Locate every Plasmodium falciparum-infected red blood cell.
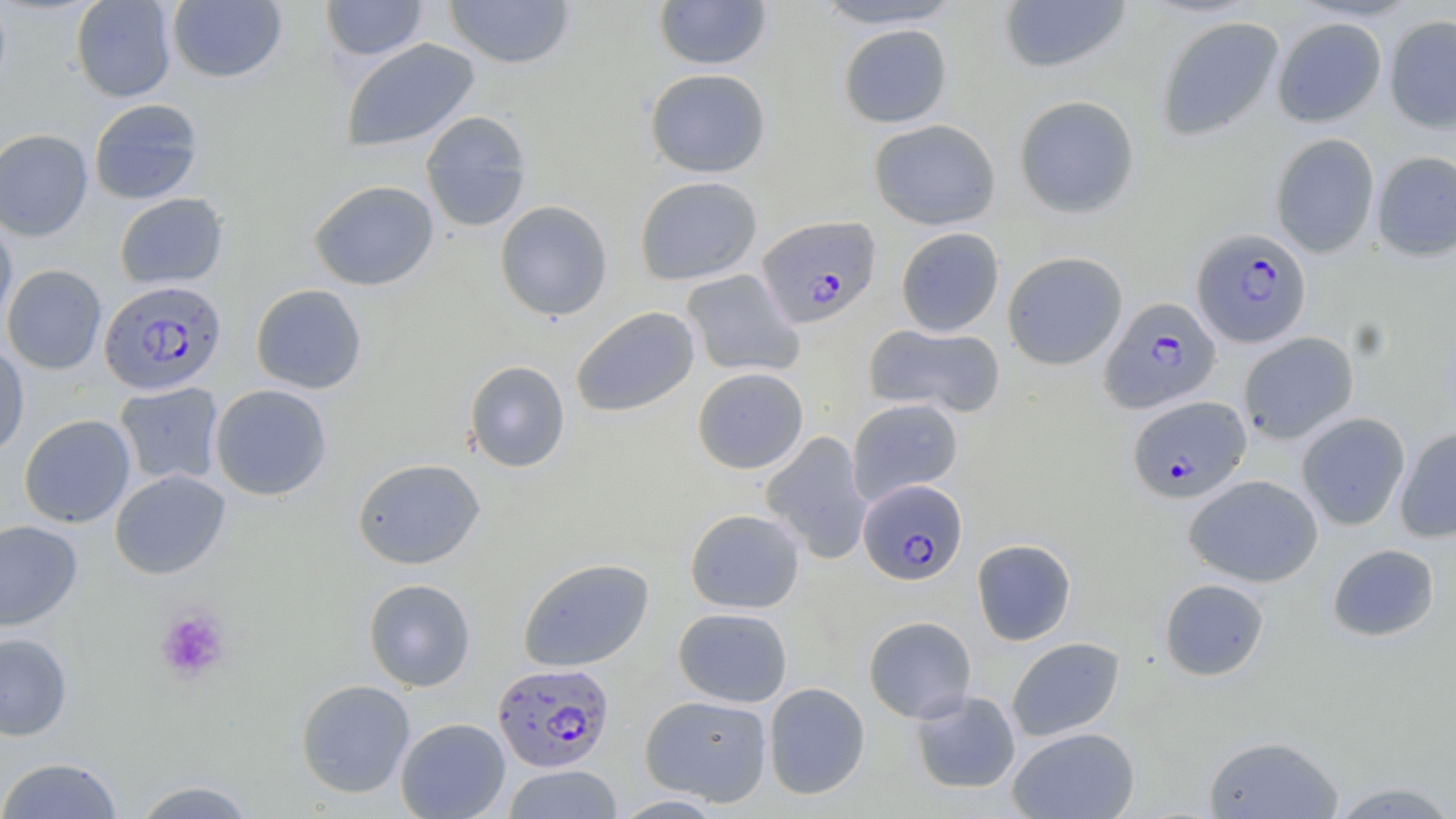
Approximate bounding boxes as (x1, y1, x2, y2) in pixels.
Plasmodium falciparum-infected red blood cells: (757, 215, 881, 328), (1191, 228, 1312, 348), (98, 280, 226, 395), (1100, 296, 1221, 414), (1127, 395, 1251, 504), (858, 479, 968, 586), (493, 661, 614, 772).

Uninfected red blood cell locations: (71, 0, 176, 102), (320, 0, 429, 61), (444, 0, 575, 69), (653, 0, 772, 70), (812, 0, 966, 29), (998, 0, 1132, 75), (167, 1, 286, 83), (1384, 15, 1456, 133), (1156, 16, 1284, 141), (1272, 17, 1387, 127), (838, 24, 952, 128), (340, 38, 480, 153), (645, 68, 771, 178), (1014, 95, 1140, 219), (88, 98, 204, 204), (420, 110, 532, 232), (869, 119, 1001, 230), (0, 129, 93, 241), (1270, 133, 1380, 258), (1372, 151, 1456, 261), (634, 175, 762, 286), (308, 179, 439, 291), (114, 192, 228, 290), (495, 200, 613, 321), (0, 217, 17, 329), (895, 227, 1004, 336), (1003, 251, 1128, 370), (2, 264, 107, 374), (681, 269, 804, 378), (250, 283, 367, 394), (571, 306, 700, 417), (864, 323, 1006, 418), (1238, 332, 1359, 444), (0, 341, 30, 458), (464, 360, 570, 473), (692, 367, 809, 473), (114, 382, 224, 487), (209, 384, 332, 501), (848, 397, 963, 504), (1296, 412, 1411, 530), (19, 414, 136, 528), (1395, 428, 1456, 543), (760, 431, 873, 563), (352, 457, 485, 570), (110, 469, 230, 579), (1184, 474, 1323, 587), (685, 508, 805, 613), (0, 520, 83, 631), (971, 539, 1077, 646), (1326, 543, 1440, 642), (517, 557, 654, 672), (363, 578, 476, 691), (1159, 578, 1270, 681), (673, 607, 793, 707), (863, 616, 977, 723), (0, 632, 73, 741), (1006, 637, 1125, 742), (295, 679, 415, 798), (763, 682, 870, 800), (910, 690, 1021, 794), (640, 694, 772, 806), (395, 717, 510, 818), (1007, 727, 1140, 818), (1202, 734, 1344, 818), (0, 757, 124, 818), (503, 764, 622, 819), (131, 778, 259, 818), (1327, 780, 1456, 818), (611, 794, 728, 817). Platelet locations: (155, 606, 231, 682). Slide-level diagnosis: Plasmodium falciparum. One field of a larger specimen. May-Grünwald-Giemsa-stained preparation. Light microscopy. Thin blood smear. Captured at 1000x magnification. Image is 1456×819 pixels.